Assess this cell for malaria.
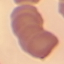

Uninfected.

stain: Giemsa
image_type: cell patch, automatically extracted from a larger field of view and resized to 64 × 64 pixels
capture: smartphone through the microscope eyepiece
preparation: thin blood smear